Locate every blood parasite and identify its species.
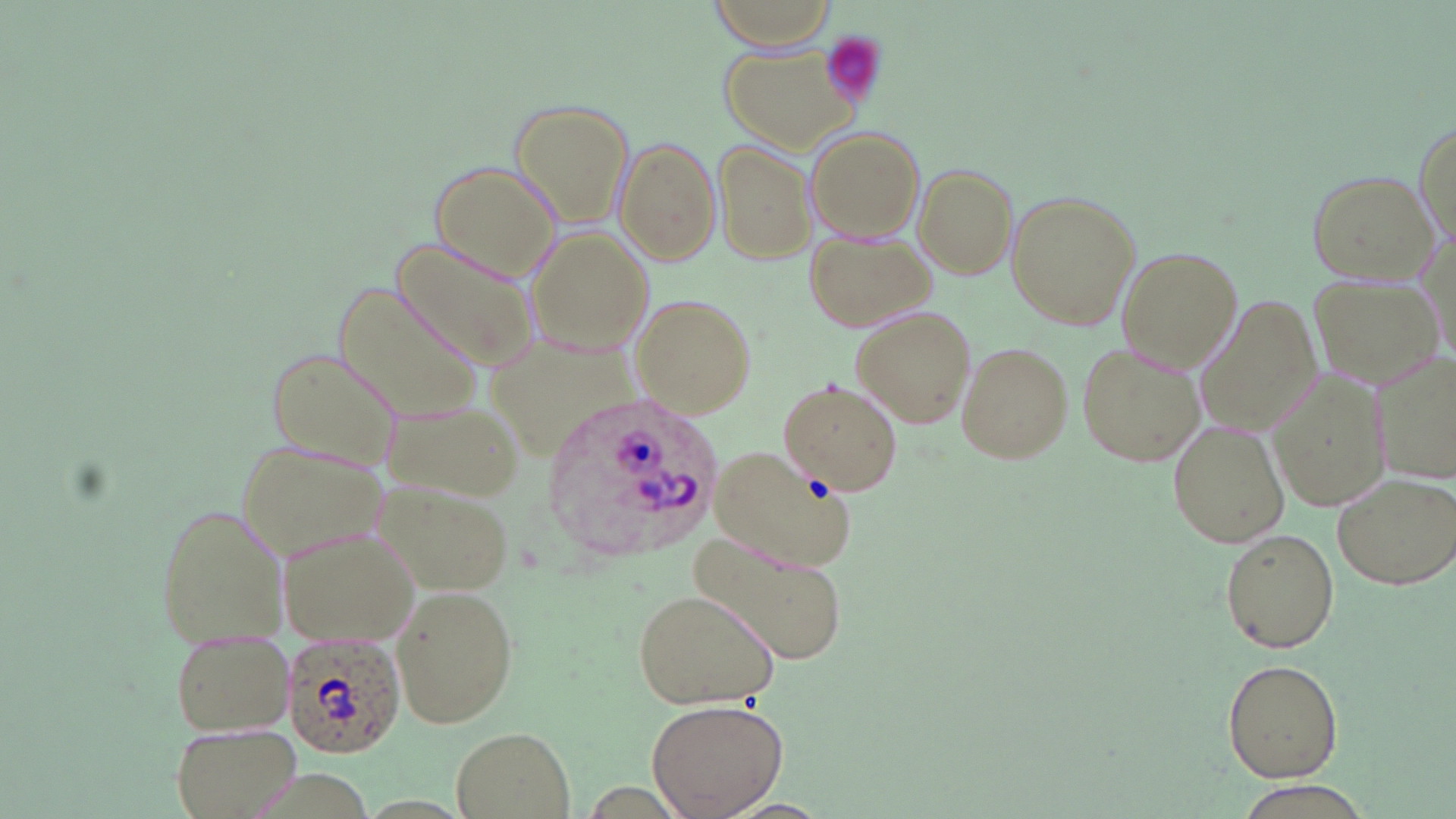
Approximate bounding boxes as (x1, y1, x2, y2) in pixels.
Plasmodium ovale-infected red blood cells: (544, 394, 727, 565), (282, 633, 406, 760).
No Plasmodium falciparum, Plasmodium malariae, Plasmodium vivax, Babesia divergens, or Trypanosoma brucei observed.

Platelet locations: (820, 34, 886, 108). Uninfected red blood cell locations: (708, 0, 840, 52), (721, 42, 859, 152), (509, 97, 635, 229), (1412, 118, 1454, 252), (803, 125, 926, 243), (616, 137, 720, 267), (714, 137, 817, 265), (428, 160, 560, 282), (913, 163, 1018, 280), (1306, 171, 1442, 285), (1005, 190, 1140, 331), (528, 228, 654, 358), (804, 230, 936, 333), (391, 239, 539, 371), (1117, 247, 1242, 375), (1311, 273, 1440, 387), (336, 279, 486, 423), (1198, 293, 1321, 437), (629, 295, 755, 421), (850, 306, 977, 430), (955, 341, 1072, 465), (1075, 341, 1206, 468), (262, 344, 405, 468), (1374, 355, 1456, 487), (1267, 368, 1392, 513), (779, 379, 903, 496), (377, 394, 525, 502), (1167, 417, 1290, 550), (236, 439, 387, 557), (711, 442, 855, 572), (1331, 472, 1456, 590), (152, 501, 290, 652), (278, 523, 423, 646), (1221, 529, 1340, 654), (693, 532, 844, 664), (386, 581, 522, 730), (630, 588, 779, 711), (165, 623, 297, 737), (1221, 659, 1343, 782), (646, 697, 789, 819), (169, 722, 301, 819), (451, 727, 575, 817), (1232, 786, 1371, 819). Slide-level diagnosis: Plasmodium ovale. May-Grünwald-Giemsa stain. Single field of view. Image is 1456×819 pixels. 1000x magnification. Light microscopy. Thin blood smear.